Name the cell type shown.
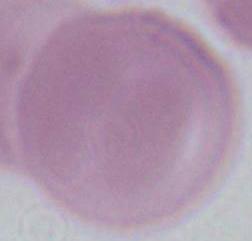
An erythrocyte.

Captured at 1000x magnification. Micrograph.